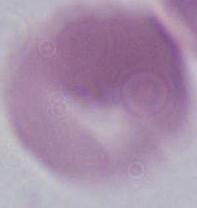
modality = photomicrograph
magnification = 1000x
identification = erythrocyte